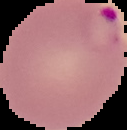 Image is 127×130 pixels. From a thin blood smear. Result: Plasmodium parasites detected. Cell region segmented out of the field of view; the surrounding area is masked to black.